Report the malaria status of this cell.
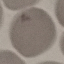

It is uninfected.

Summary:
  - Preparation: thin blood film
  - Stain: Giemsa
  - Capture: smartphone camera at the microscope eyepiece
  - Image type: automatically extracted cell patch, resized to 64 × 64 pixels